Assess the morphology of the erythrocytes.
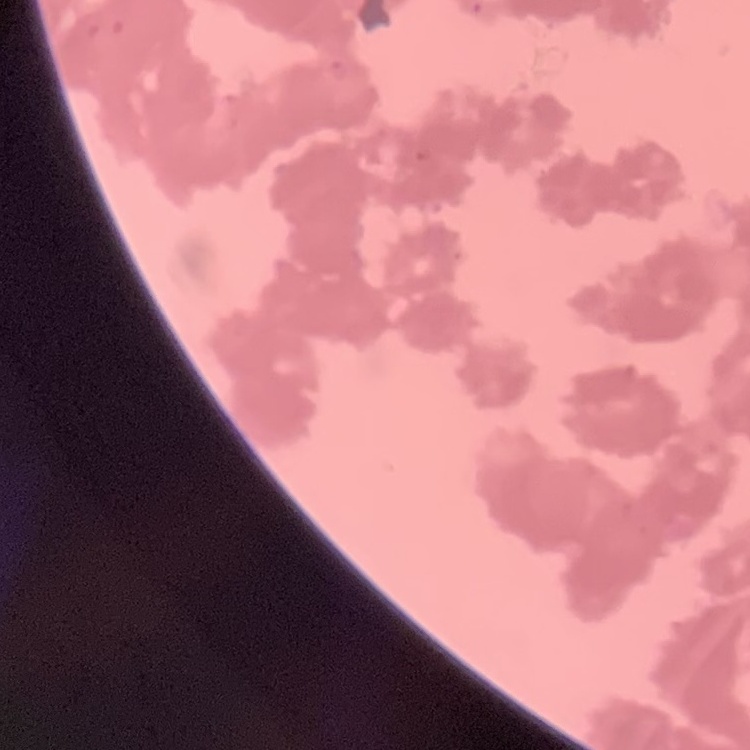

Rouleaux formation.

Thin blood film. Square crop of a larger photomicrograph. Stained with either Field's or Giemsa.